Classify this cell by malaria status.
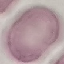

Uninfected.

Summary:
  - Capture: smartphone camera at the microscope eyepiece
  - Image type: automatically extracted cell patch, resized to 64 × 64 pixels
  - Preparation: thin blood smear
  - Stain: Giemsa